Give the position of every Plasmodium parasite visible.
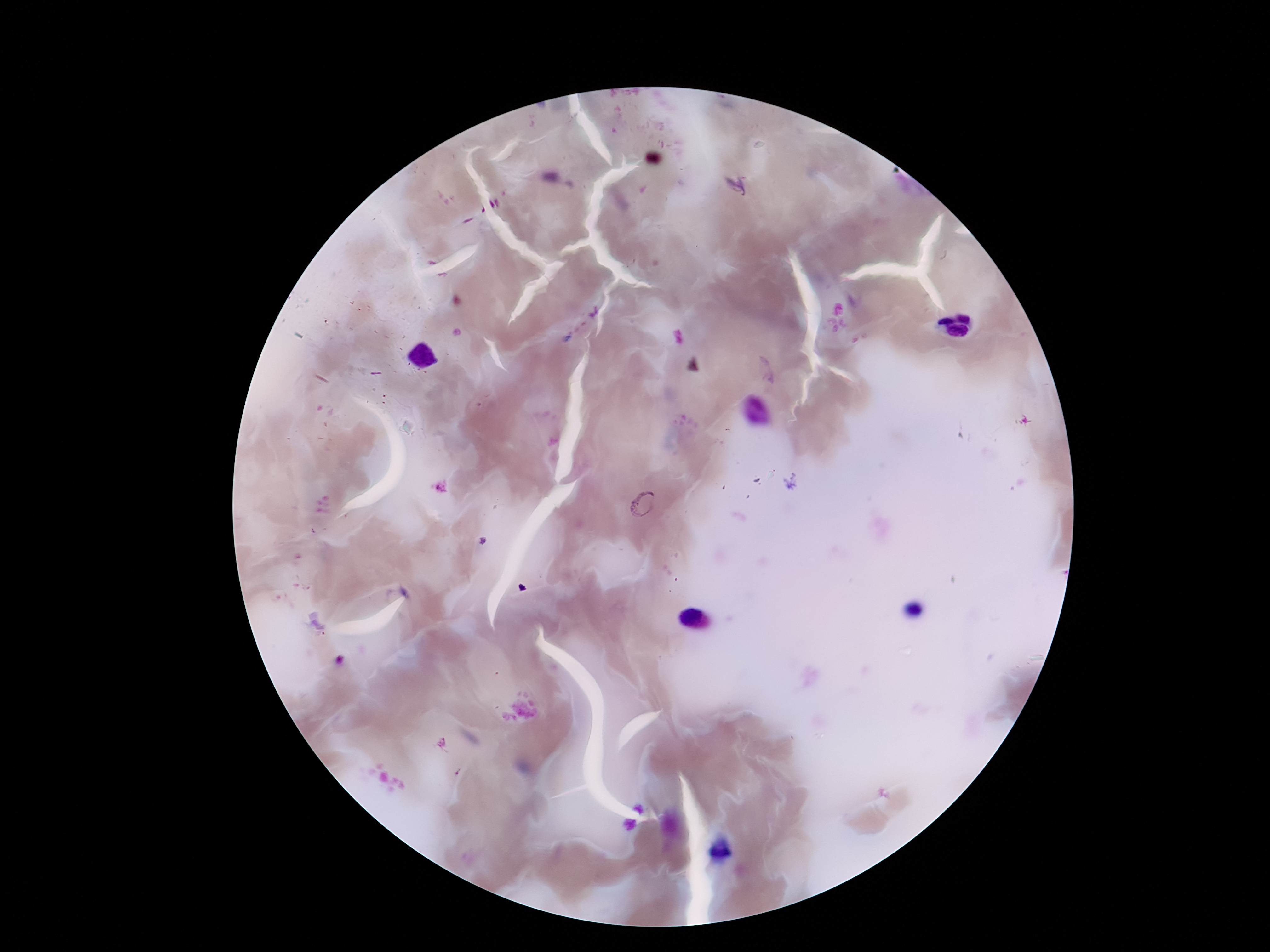

Approximate centers as {x, y} in pixels.
Plasmodium parasites: {736, 187}, {644, 504}.

image_size: 1270×952 pixels
magnification: 100x
preparation: thick blood smear
stain: Giemsa
field_of_view: single
patient_malaria_status: positive
capture: smartphone camera through the microscope eyepiece